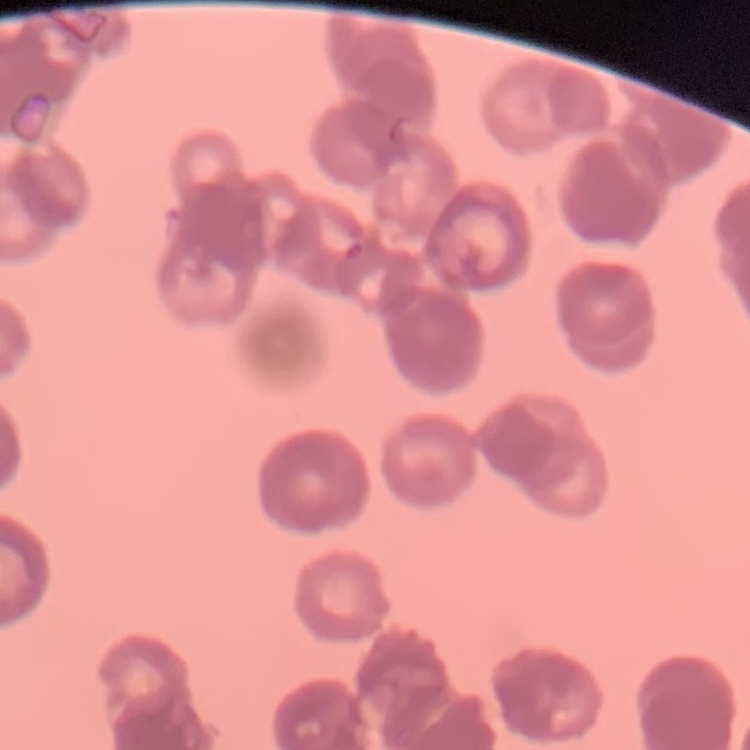
red blood cell morphology = rouleaux formation
image type = one tile cut from a larger photomicrograph
preparation = thin blood smear
stain = Field's or Giemsa